State which parasite is depicted.
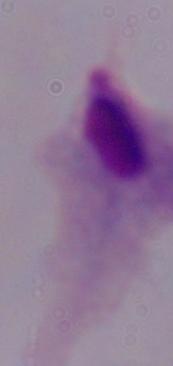

A trichomonad.

Summary:
  - Magnification: 1000x
  - Modality: micrograph